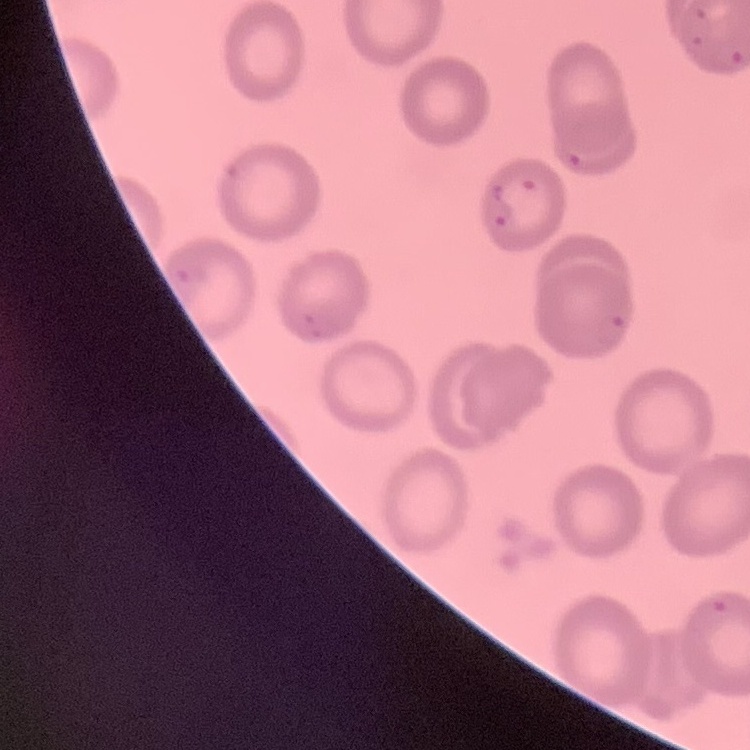
The red blood cells exhibit no rouleaux formation. Stained with either Field's or Giemsa. Square crop of a larger photomicrograph. Thin peripheral smear.